Locate every Plasmodium parasite.
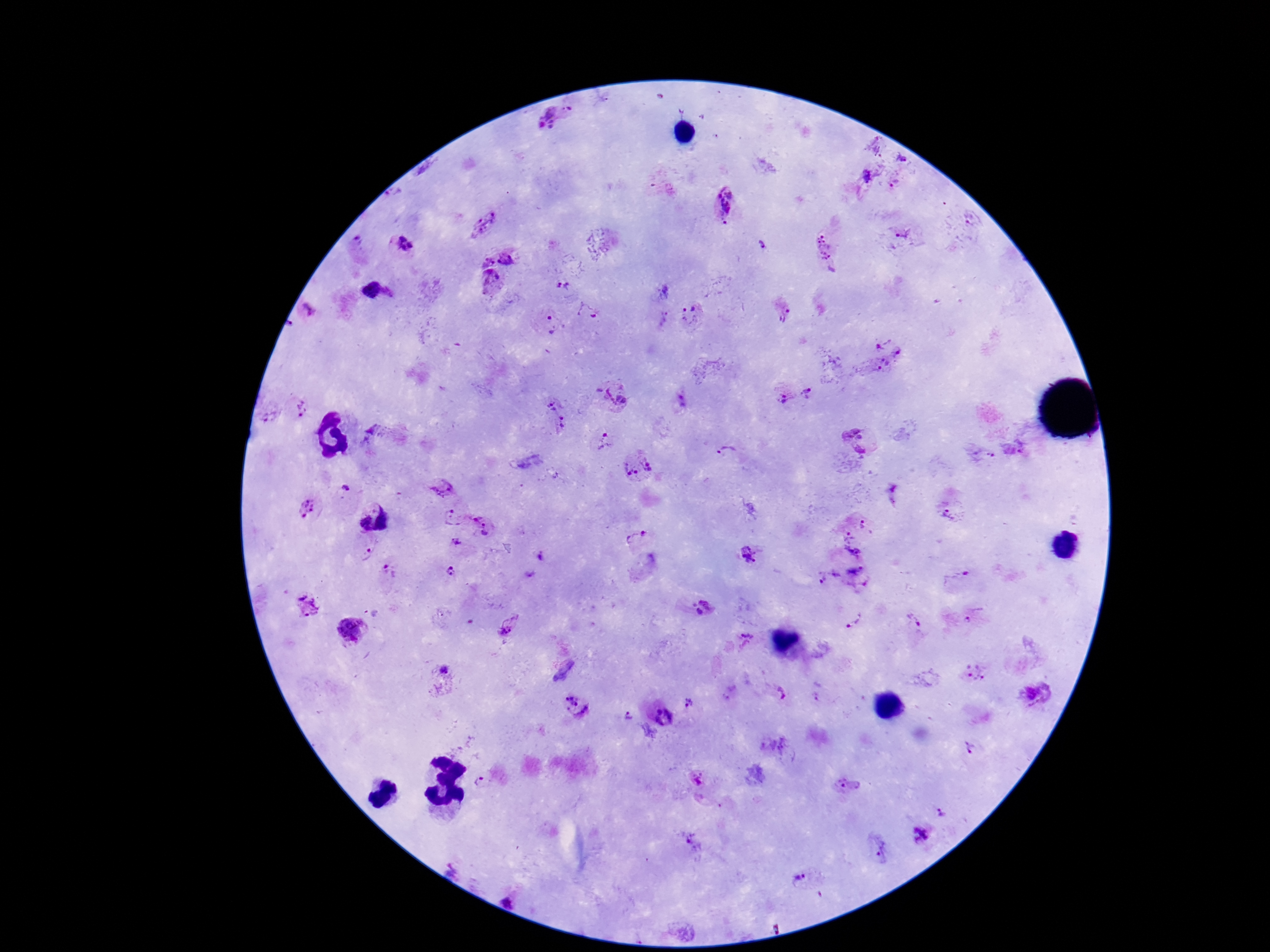
Approximate centers as (x, y) in pixels.
Plasmodium parasites: (560, 121), (901, 159), (867, 178), (894, 184), (721, 202), (971, 218), (482, 221), (905, 234), (358, 245), (402, 245), (763, 245), (827, 250), (511, 256), (483, 259), (494, 283), (562, 287), (373, 291), (308, 309), (587, 312), (784, 314), (691, 316), (664, 320), (553, 326), (879, 342), (897, 351), (878, 364), (614, 394), (807, 394), (785, 398), (553, 402), (303, 407), (562, 422), (857, 439), (604, 442), (1016, 447), (729, 454), (983, 457), (638, 465), (443, 488), (346, 491), (893, 493), (309, 509), (950, 511), (388, 518), (452, 518), (361, 523), (486, 524), (867, 524), (644, 534), (846, 536), (629, 541), (460, 542), (853, 553), (366, 554), (747, 555), (539, 557), (388, 571), (453, 571), (528, 573), (954, 577), (827, 578), (858, 580), (308, 609), (703, 609), (976, 614), (856, 619), (912, 619), (511, 626), (353, 630), (747, 636), (561, 665), (447, 668), (974, 671), (779, 694), (1038, 694), (819, 698), (688, 704), (575, 706), (664, 717), (626, 720), (969, 749), (698, 779), (484, 781), (848, 787), (942, 814), (918, 835), (693, 843), (880, 849), (798, 883).

Summary:
  - Stain: Giemsa
  - Capture: smartphone camera through the microscope eyepiece
  - Image size: 1270×952 pixels
  - Preparation: thick blood film
  - Patient malaria status: infected
  - Magnification: 100x
  - Field of view: single